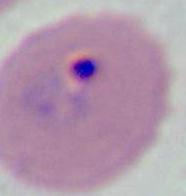

modality = micrograph
identification = Plasmodium
magnification = 400x or 1000x